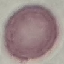
result: negative for malaria parasites
preparation: thin blood smear
stain: Giemsa
capture: smartphone camera at the microscope eyepiece
image_type: automatically extracted cell patch, resized to 64 × 64 pixels